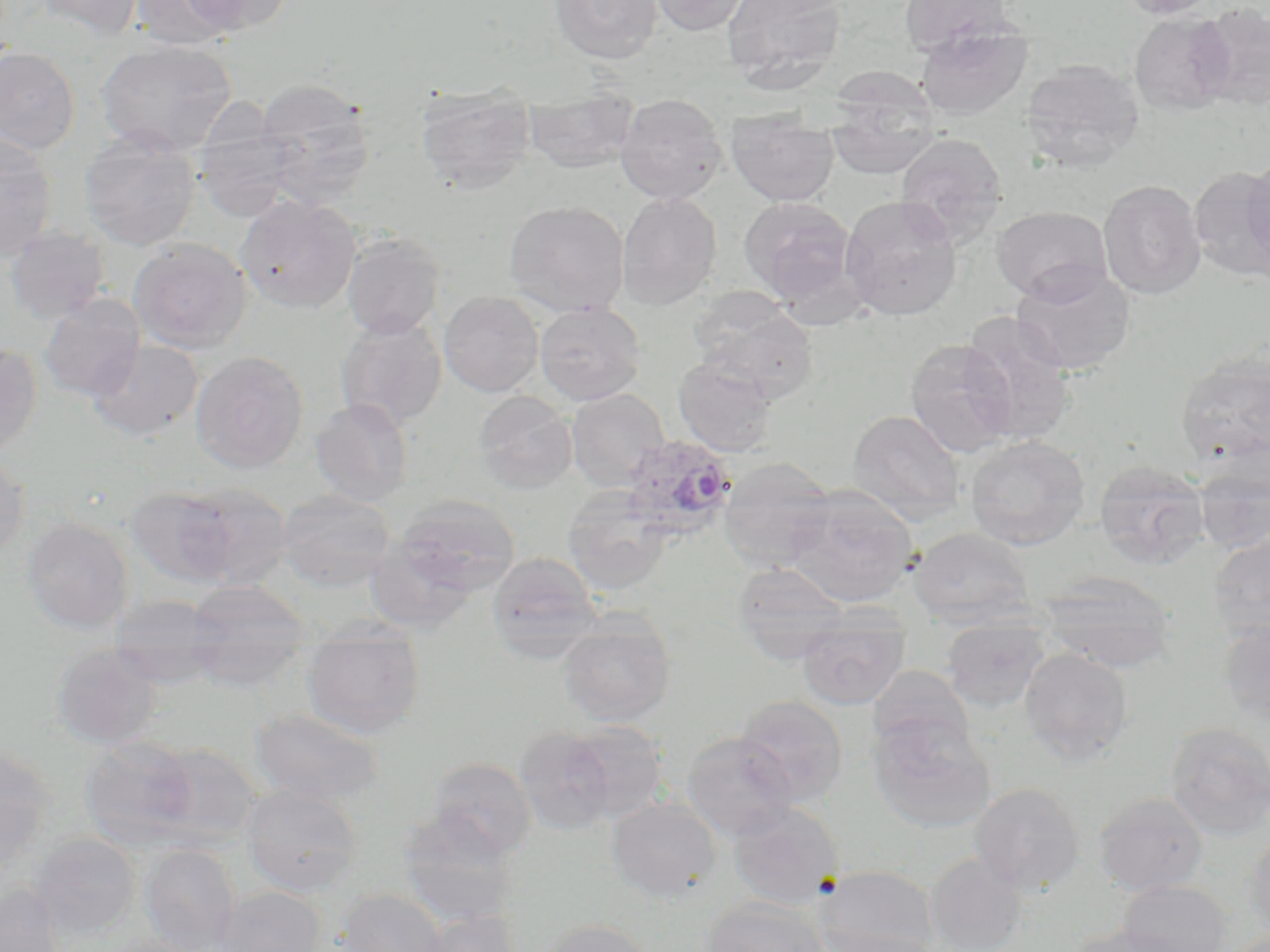
slide-level diagnosis = Plasmodium ovale
magnification = 1000x
preparation = thin blood smear
Plasmodium ovale-infected red blood cell locations = approximate bounding boxes as named x1/y1/x2/y2 corners in pixels: (x1=621, y1=434, x2=738, y2=540)
image size = 1270×952 pixels
modality = optical microscopy
stain = May-Grünwald-Giemsa
field of view = one of a larger specimen
uninfected red blood cell locations = approximate bounding boxes as named x1/y1/x2/y2 corners in pixels: (x1=33, y1=0, x2=145, y2=40), (x1=131, y1=0, x2=241, y2=51), (x1=179, y1=0, x2=293, y2=34), (x1=550, y1=0, x2=662, y2=64), (x1=647, y1=0, x2=753, y2=36), (x1=721, y1=0, x2=847, y2=87), (x1=898, y1=0, x2=1012, y2=55), (x1=1116, y1=0, x2=1218, y2=20), (x1=1194, y1=4, x2=1270, y2=110), (x1=1129, y1=12, x2=1236, y2=116), (x1=915, y1=26, x2=1033, y2=121), (x1=95, y1=40, x2=237, y2=157), (x1=0, y1=47, x2=80, y2=154), (x1=1020, y1=58, x2=1145, y2=169), (x1=825, y1=75, x2=941, y2=181), (x1=256, y1=79, x2=376, y2=205), (x1=416, y1=86, x2=535, y2=194), (x1=523, y1=88, x2=638, y2=174), (x1=616, y1=93, x2=728, y2=204), (x1=726, y1=109, x2=838, y2=206), (x1=193, y1=113, x2=299, y2=222), (x1=0, y1=131, x2=57, y2=261), (x1=895, y1=132, x2=1008, y2=243), (x1=79, y1=133, x2=199, y2=251), (x1=1242, y1=153, x2=1270, y2=274), (x1=1190, y1=166, x2=1270, y2=283), (x1=1098, y1=179, x2=1206, y2=300), (x1=616, y1=192, x2=722, y2=310), (x1=236, y1=194, x2=361, y2=313), (x1=839, y1=195, x2=963, y2=322), (x1=739, y1=196, x2=857, y2=304), (x1=504, y1=200, x2=629, y2=317), (x1=991, y1=205, x2=1112, y2=303), (x1=4, y1=225, x2=110, y2=324), (x1=342, y1=233, x2=444, y2=339), (x1=129, y1=237, x2=252, y2=354), (x1=1011, y1=264, x2=1136, y2=376), (x1=687, y1=289, x2=820, y2=402), (x1=438, y1=291, x2=544, y2=397), (x1=39, y1=294, x2=145, y2=401), (x1=534, y1=301, x2=646, y2=405), (x1=959, y1=311, x2=1076, y2=445), (x1=335, y1=316, x2=447, y2=429), (x1=905, y1=338, x2=1018, y2=457), (x1=87, y1=339, x2=203, y2=441), (x1=0, y1=343, x2=42, y2=457), (x1=191, y1=350, x2=308, y2=473), (x1=1175, y1=351, x2=1270, y2=468), (x1=673, y1=357, x2=778, y2=457), (x1=566, y1=388, x2=670, y2=491), (x1=473, y1=390, x2=578, y2=495), (x1=310, y1=398, x2=413, y2=506), (x1=846, y1=409, x2=966, y2=525), (x1=965, y1=436, x2=1089, y2=550), (x1=0, y1=451, x2=29, y2=559), (x1=718, y1=457, x2=837, y2=571), (x1=1094, y1=458, x2=1210, y2=569), (x1=1192, y1=458, x2=1270, y2=553), (x1=167, y1=482, x2=294, y2=590), (x1=784, y1=485, x2=918, y2=607), (x1=125, y1=486, x2=243, y2=587), (x1=277, y1=488, x2=395, y2=591), (x1=563, y1=488, x2=674, y2=596), (x1=389, y1=495, x2=521, y2=597), (x1=21, y1=516, x2=135, y2=634), (x1=908, y1=526, x2=1034, y2=625), (x1=1208, y1=532, x2=1270, y2=639), (x1=487, y1=552, x2=601, y2=652), (x1=732, y1=563, x2=849, y2=661), (x1=1039, y1=570, x2=1178, y2=673), (x1=187, y1=580, x2=312, y2=644), (x1=107, y1=596, x2=231, y2=656), (x1=305, y1=615, x2=426, y2=645), (x1=941, y1=616, x2=1050, y2=713), (x1=1216, y1=618, x2=1270, y2=725), (x1=559, y1=619, x2=675, y2=725), (x1=797, y1=623, x2=909, y2=709), (x1=106, y1=643, x2=227, y2=687), (x1=301, y1=643, x2=425, y2=739), (x1=49, y1=645, x2=163, y2=748), (x1=183, y1=645, x2=307, y2=690), (x1=1019, y1=648, x2=1134, y2=765), (x1=868, y1=666, x2=976, y2=762), (x1=734, y1=695, x2=849, y2=803), (x1=250, y1=708, x2=383, y2=807), (x1=868, y1=716, x2=996, y2=834), (x1=563, y1=721, x2=668, y2=822), (x1=1164, y1=722, x2=1269, y2=840), (x1=514, y1=725, x2=616, y2=834), (x1=682, y1=731, x2=799, y2=841), (x1=80, y1=738, x2=199, y2=851), (x1=146, y1=742, x2=261, y2=849), (x1=0, y1=745, x2=54, y2=864), (x1=426, y1=757, x2=537, y2=861), (x1=970, y1=782, x2=1086, y2=894), (x1=241, y1=783, x2=362, y2=897), (x1=1093, y1=791, x2=1208, y2=894), (x1=606, y1=797, x2=721, y2=902), (x1=727, y1=801, x2=844, y2=909), (x1=398, y1=813, x2=518, y2=925), (x1=1245, y1=831, x2=1270, y2=940), (x1=30, y1=833, x2=141, y2=939), (x1=140, y1=844, x2=241, y2=952), (x1=925, y1=852, x2=1028, y2=952), (x1=812, y1=864, x2=940, y2=951), (x1=1117, y1=880, x2=1232, y2=952), (x1=0, y1=882, x2=65, y2=952), (x1=213, y1=886, x2=327, y2=952), (x1=336, y1=888, x2=448, y2=952), (x1=701, y1=897, x2=830, y2=952), (x1=414, y1=909, x2=522, y2=952), (x1=538, y1=919, x2=657, y2=952), (x1=1065, y1=923, x2=1187, y2=952), (x1=826, y1=932, x2=949, y2=952)